Locate every Plasmodium parasite.
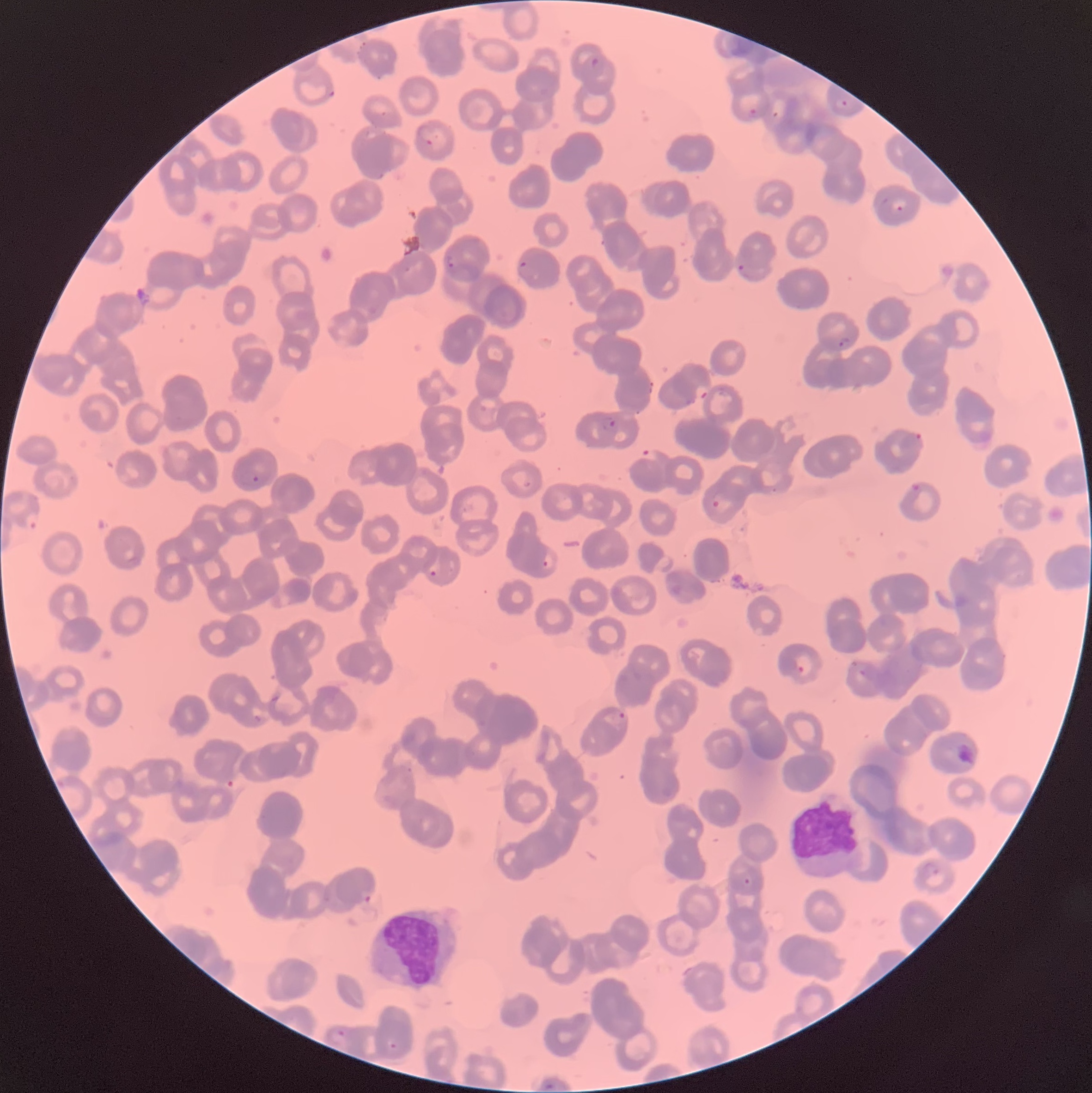

Approximate bounding boxes as (x1, y1, x2, y2) in pixels.
Plasmodium parasites: (591, 57, 599, 67), (326, 87, 335, 100), (836, 98, 848, 110), (746, 105, 767, 118), (416, 122, 435, 147), (896, 204, 904, 213), (445, 254, 457, 270), (519, 261, 535, 282), (737, 262, 745, 274), (404, 264, 415, 274), (837, 337, 850, 349), (600, 417, 618, 432), (913, 433, 924, 445), (640, 449, 658, 463), (251, 474, 260, 484), (910, 483, 921, 493), (711, 499, 722, 509), (23, 510, 40, 531), (541, 559, 549, 568), (429, 570, 438, 578), (797, 665, 805, 673), (858, 668, 867, 678), (618, 711, 627, 720), (920, 861, 941, 877), (743, 878, 751, 885), (361, 889, 374, 904), (336, 1028, 347, 1038), (389, 1042, 397, 1049), (544, 1082, 557, 1091).

White blood cell locations: (369, 909, 458, 990). The red blood cells show rouleaux formation. Thin blood smear. Optical microscopy. Image is 1092×1093 pixels.